Point out every Plasmodium parasite and every leukocyte.
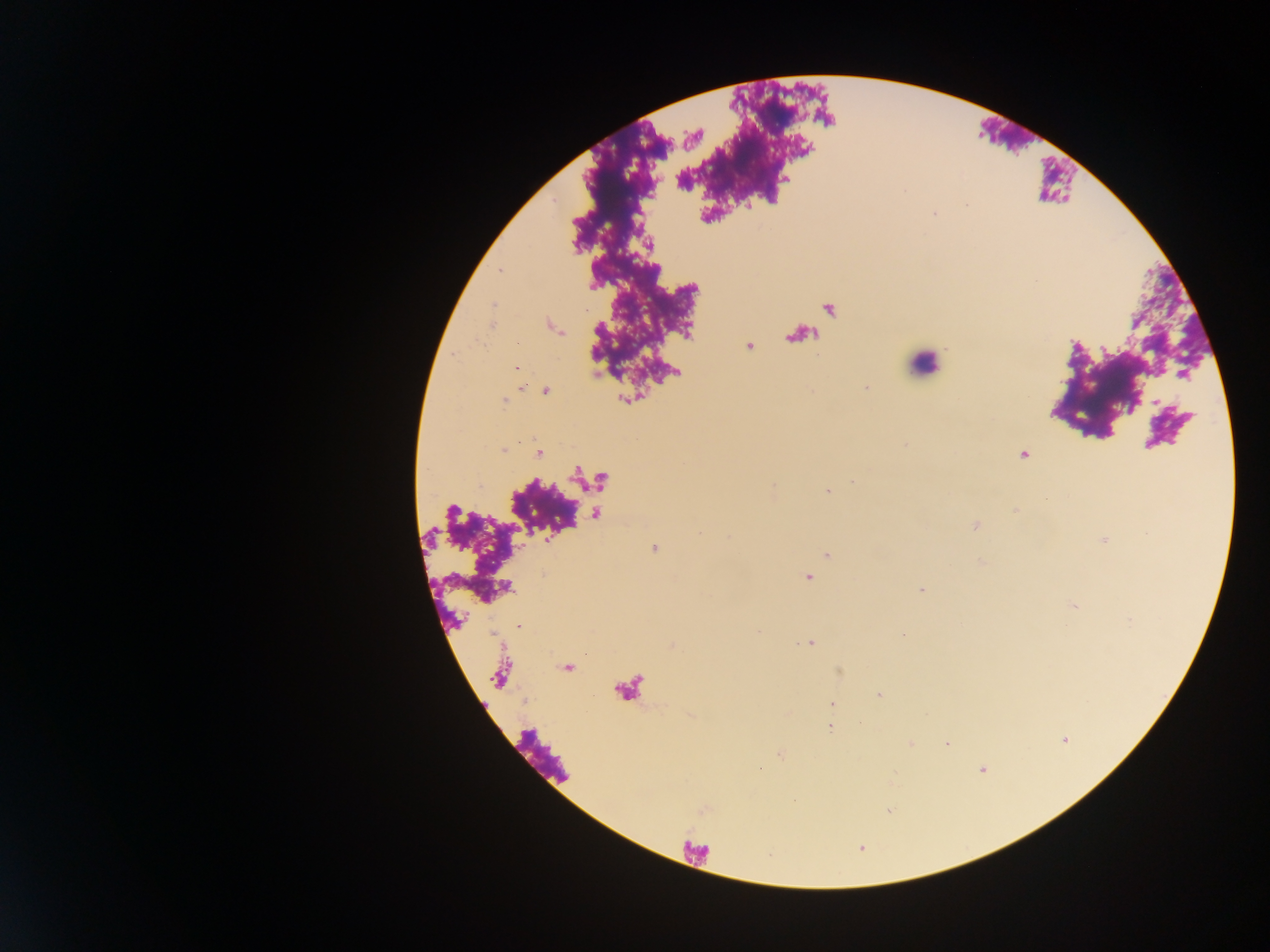

Approximate centers as {x, y} in pixels.
Plasmodium parasites: {935, 214}, {649, 244}, {500, 271}, {517, 367}, {866, 388}, {546, 391}, {1157, 403}, {503, 451}, {538, 453}, {1024, 454}, {852, 482}, {826, 492}, {1046, 499}, {1015, 511}, {975, 526}, {699, 533}, {654, 548}, {828, 555}, {808, 578}, {921, 590}, {518, 626}, {758, 633}, {810, 643}, {879, 696}, {831, 704}, {830, 727}, {947, 744}, {780, 754}, {759, 768}, {982, 770}.
Leukocytes: {924, 364}.

Single field of view. Collected in Ghana. Photographed through a microscope with a mobile-phone camera. Thick blood film. Image is 1270×952 pixels.